Describe the morphology of the red blood cells.
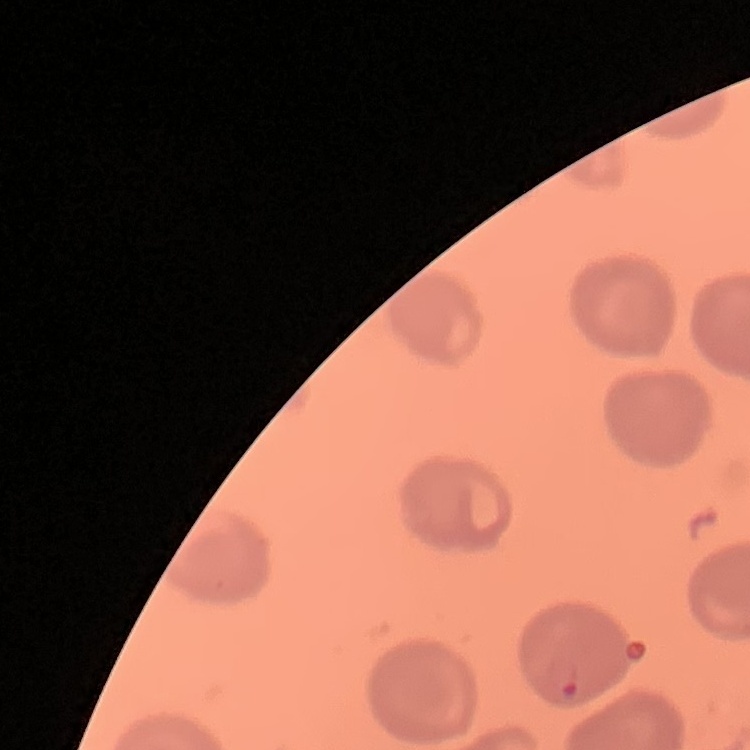

No rouleaux formation.

{
  "stain": "Field's or Giemsa",
  "preparation": "thin blood film",
  "image_type": "one tile cut from a larger photomicrograph"
}